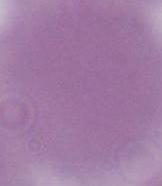

{
  "magnification": "1000x",
  "modality": "micrograph",
  "identification": "red blood cell"
}